Assess the morphology of the erythrocytes.
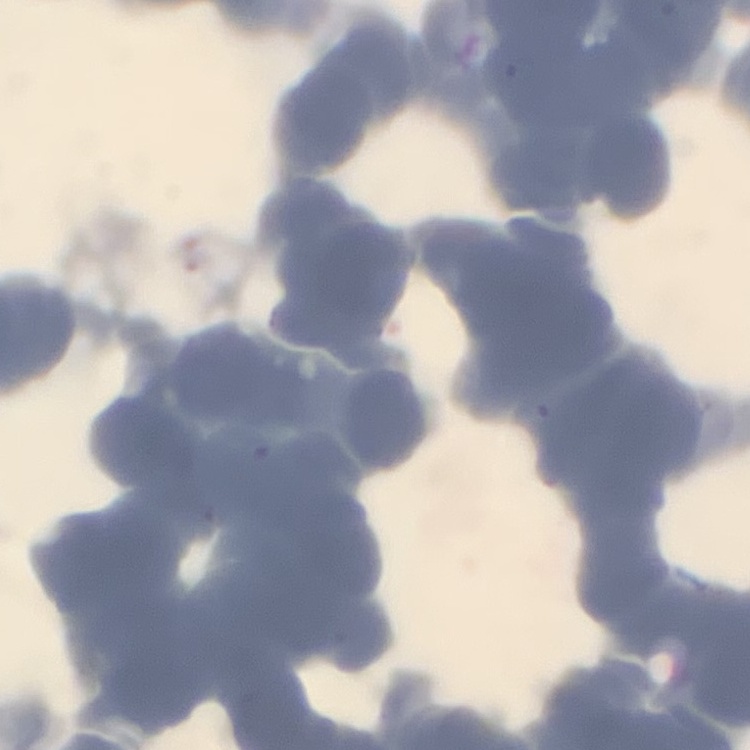

Rouleaux formation.

Summary:
  - Image type: one tile cut from a larger photomicrograph
  - Stain: Field's or Giemsa
  - Preparation: thin blood smear